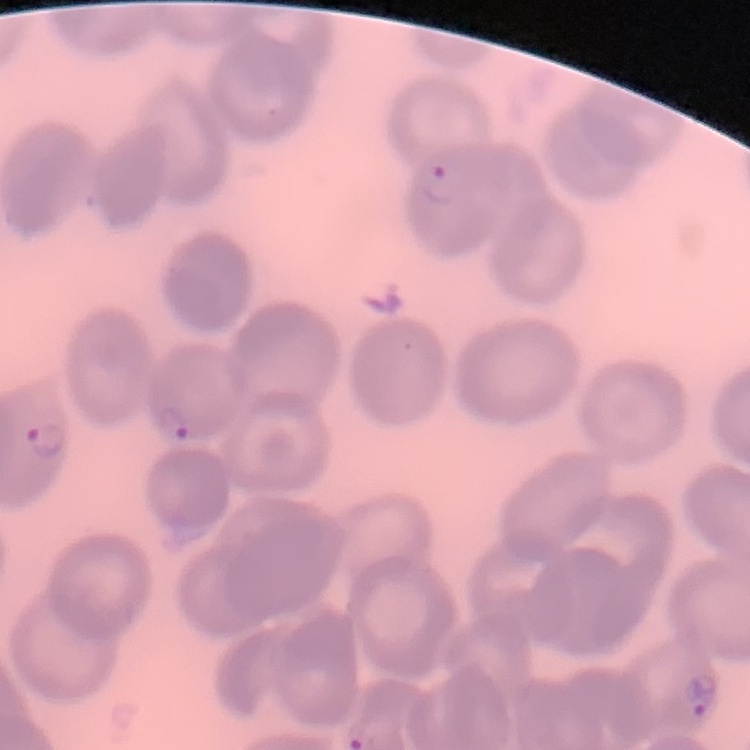
red blood cell morphology = no rouleaux formation
stain = Field's or Giemsa
image type = one tile cut from a larger photomicrograph
preparation = thin blood smear